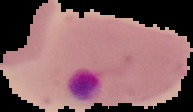
Summary:
  - Malaria status: parasitized
  - Image type: segmented cell region with the area outside set to black
  - Preparation: thin blood smear
  - Image size: 193×112 pixels